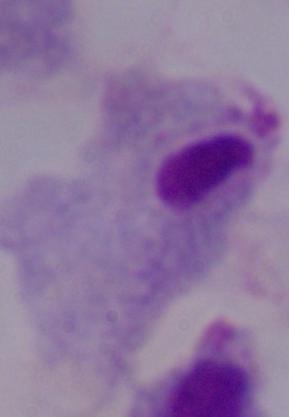

1000x magnification. A trichomonad is shown. Photomicrograph.